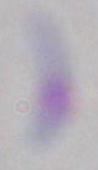

Summary:
  - Modality: micrograph
  - Identification: Toxoplasma gondii
  - Magnification: 1000x